Locate every Plasmodium malariae-infected red blood cell.
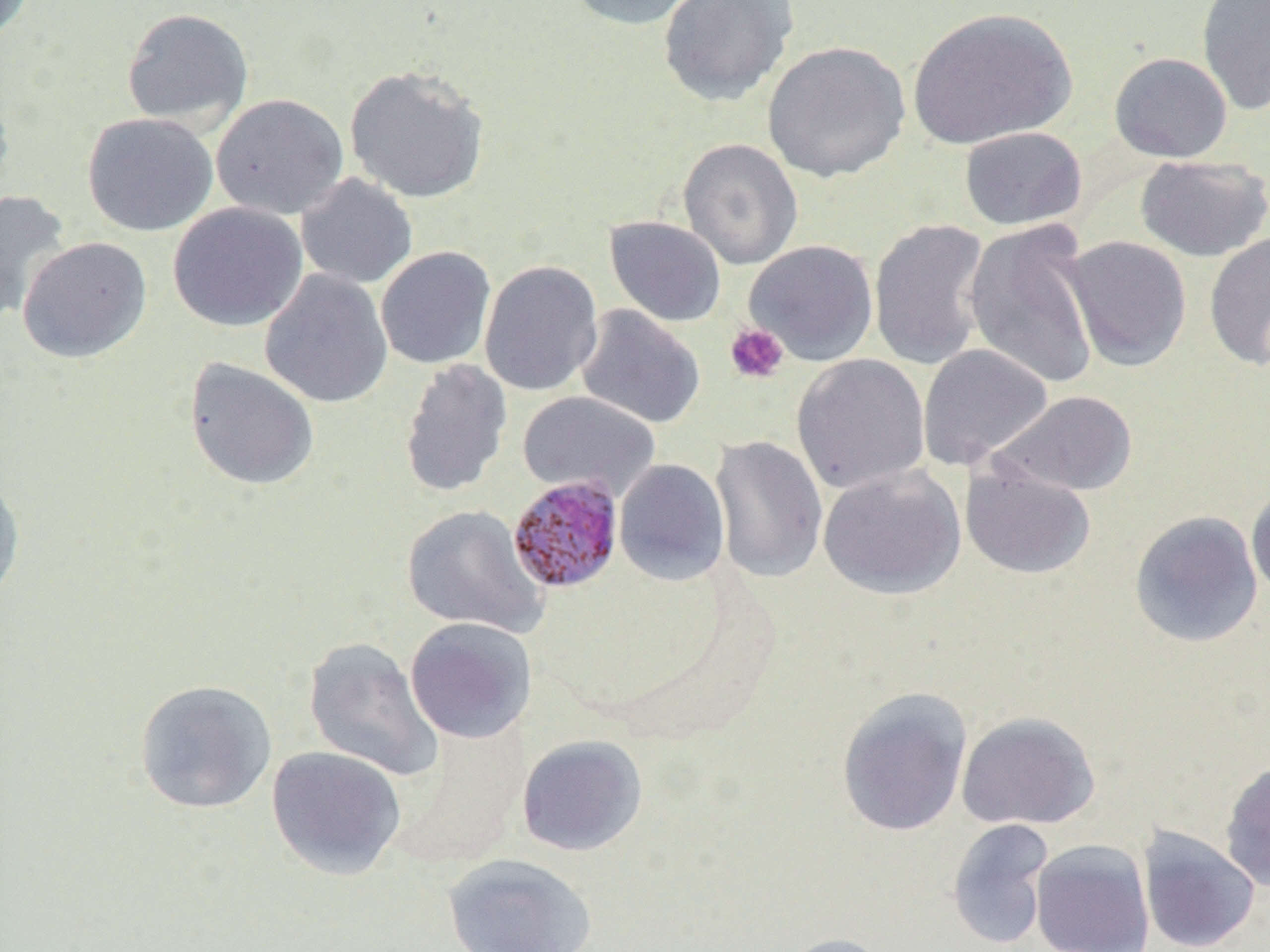
Approximate bounding boxes as (x1,y1)-(x2,y2) corner pairs in pixels.
Plasmodium malariae-infected red blood cells: (507,475)-(624,594).

slide-level diagnosis = Plasmodium malariae
modality = optical microscopy
magnification = 1000x
uninfected red blood cell locations = approximate bounding boxes as (x1,y1)-(x2,y2) corner pairs in pixels: (0,0)-(36,46), (565,0)-(708,31), (657,0)-(798,107), (1196,0)-(1270,117), (121,6)-(254,130), (906,6)-(1076,150), (762,40)-(911,183), (1109,52)-(1233,163), (344,65)-(491,204), (0,79)-(15,199), (210,93)-(349,220), (81,112)-(218,237), (959,126)-(1087,230), (677,138)-(803,270), (1134,155)-(1269,262), (295,173)-(418,289), (0,190)-(72,322), (167,202)-(308,332), (604,215)-(727,327), (869,218)-(991,371), (964,221)-(1101,391), (1203,232)-(1270,370), (1061,235)-(1192,372), (17,237)-(152,363), (744,240)-(878,366), (375,246)-(496,370), (479,260)-(604,397), (259,270)-(393,408), (575,305)-(706,429), (917,343)-(1053,471), (791,354)-(930,494), (184,357)-(320,491), (399,358)-(513,499), (517,390)-(660,501), (993,390)-(1138,497), (709,435)-(828,584), (614,459)-(730,586), (960,459)-(1096,580), (818,464)-(966,599), (0,473)-(25,606), (1246,484)-(1270,602), (401,505)-(547,637), (1129,510)-(1264,648), (404,617)-(537,743), (302,637)-(444,783), (134,678)-(278,814), (836,687)-(973,837), (956,711)-(1101,830), (516,735)-(648,856), (267,746)-(407,880), (1219,759)-(1270,892), (946,818)-(1055,950), (1137,826)-(1261,952), (1030,839)-(1155,952), (441,852)-(598,952), (775,932)-(894,952)
image size = 1270×952 pixels
field of view = one of a larger specimen
platelet locations = approximate bounding boxes as (x1,y1)-(x2,y2) corner pairs in pixels: (724,322)-(789,385)
preparation = thin blood film